Comment on the morphology of the erythrocytes.
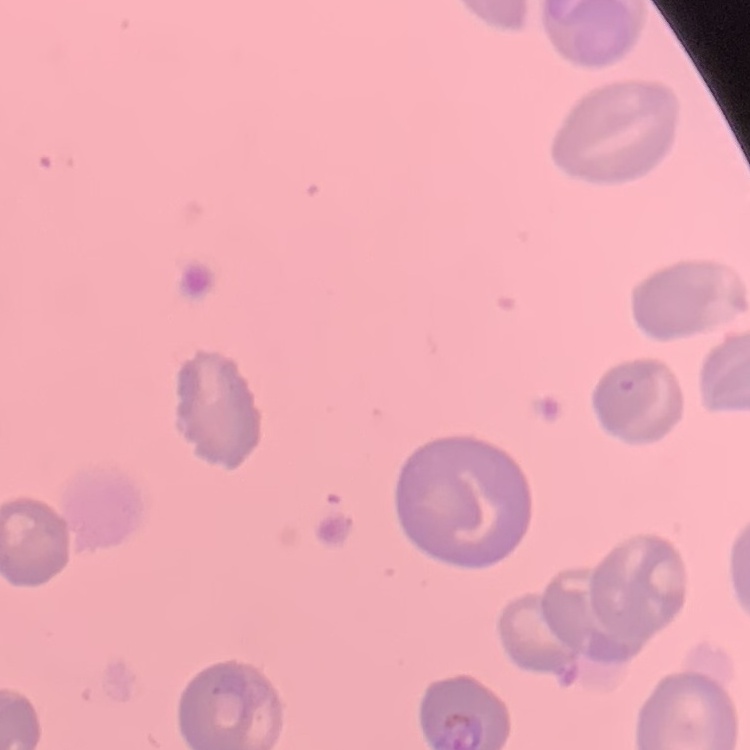

They show no rouleaux formation.

{
  "preparation": "thin blood smear",
  "stain": "Field's or Giemsa",
  "image_type": "square crop of a larger photomicrograph"
}